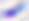

magnification: 400x
identification: Toxoplasma gondii
modality: photomicrograph